Assess this cell for malaria.
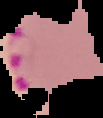
Parasitized.

From a thin blood film. Image is 103×118 pixels. Cell region segmented out of the field of view; the surrounding area is masked to black.